Report the malaria status of this cell.
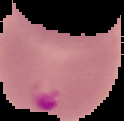

Parasitized.

image_type: segmented cell region on a black background
preparation: thin blood film
image_size: 124×121 pixels